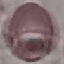

{
  "malaria_status": "uninfected",
  "preparation": "thin smear",
  "image_type": "cell patch, automatically extracted from a larger field of view and resized to 64 × 64 pixels",
  "stain": "Giemsa",
  "capture": "smartphone through the microscope eyepiece"
}